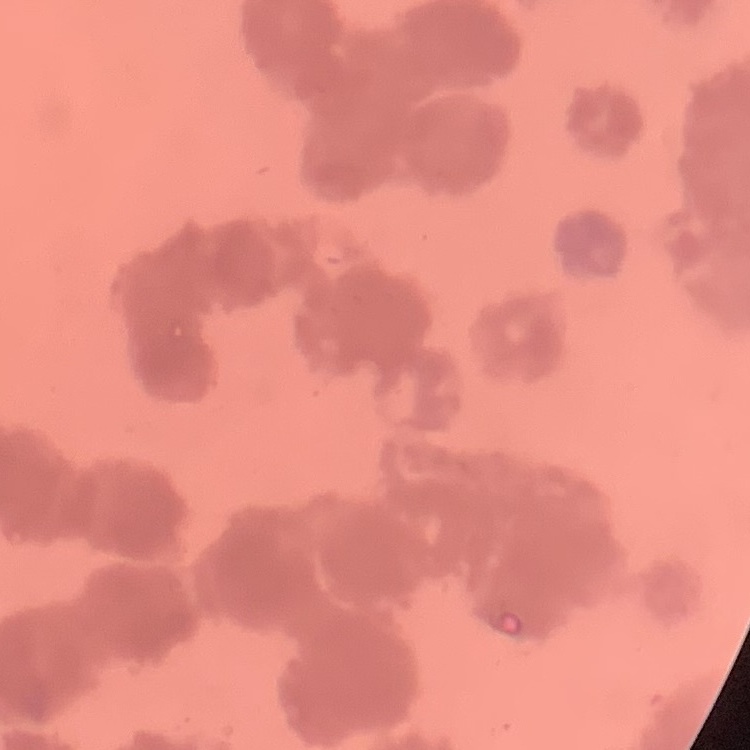 The erythrocytes show rouleaux formation. One tile cut from a larger photomicrograph. Thin blood smear. Stained with either Field's or Giemsa.